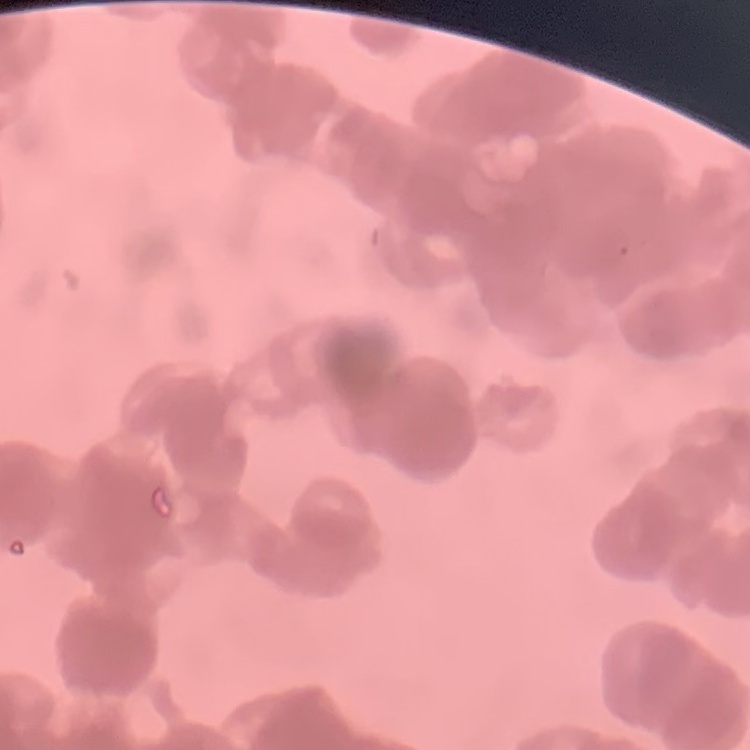

erythrocyte morphology = rouleaux formation
stain = Field's or Giemsa
image type = square crop of a larger photomicrograph
preparation = thin blood film